Give the extent of all Plasmodium vivax-infected red blood cells.
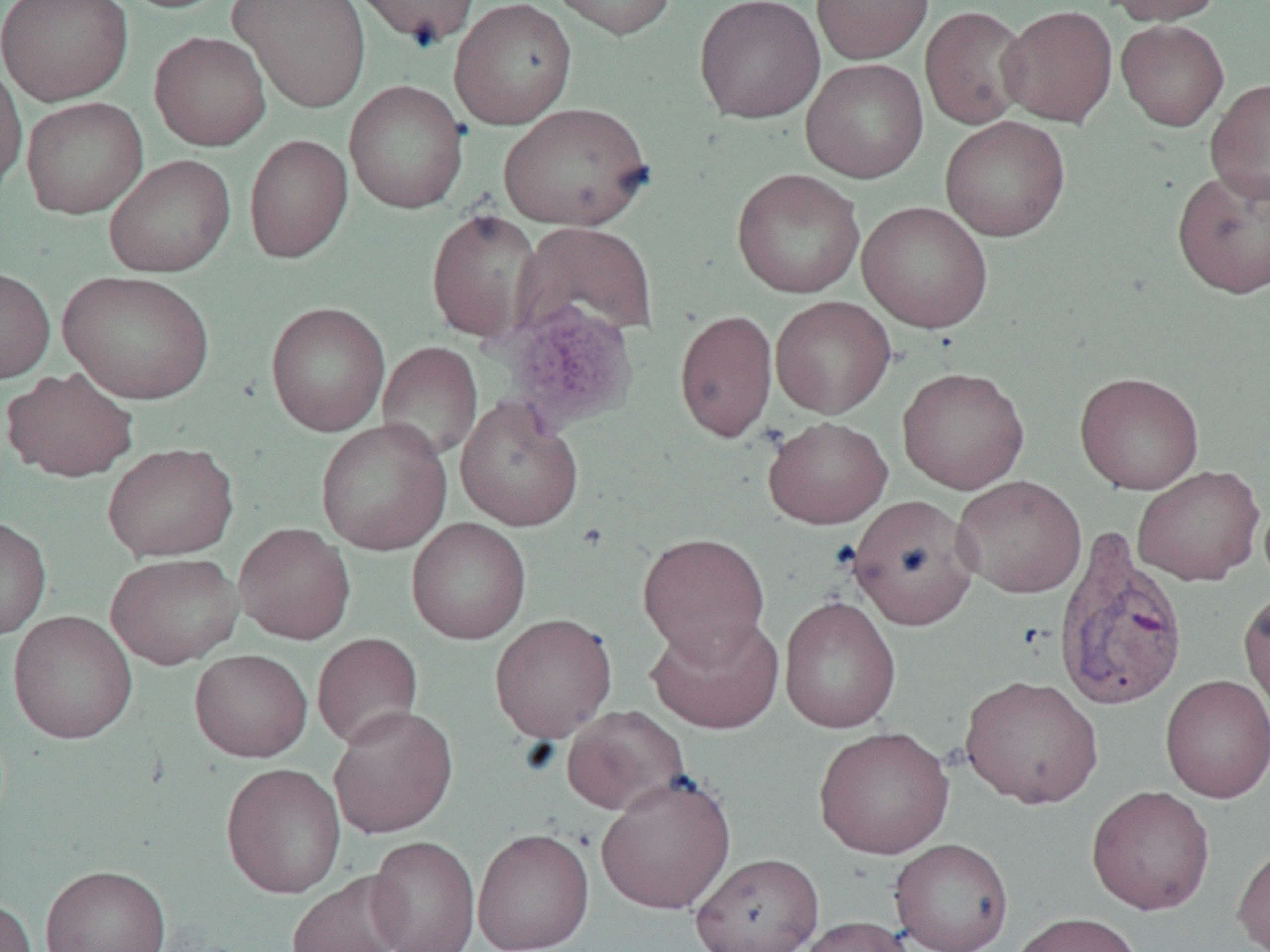

Approximate bounding boxes as [x1, y1, x2, y2] in pixels.
Plasmodium vivax-infected red blood cells: [1053, 529, 1189, 712].

Summary:
  - Platelet locations: [499, 301, 641, 434]
  - Uninfected red blood cell locations: [1, 0, 133, 106], [112, 0, 237, 14], [228, 0, 372, 114], [346, 0, 481, 48], [448, 0, 577, 129], [545, 0, 678, 40], [694, 0, 825, 124], [811, 0, 934, 63], [1103, 0, 1224, 25], [920, 5, 1032, 130], [998, 5, 1118, 127], [1116, 19, 1229, 131], [149, 31, 271, 151], [800, 58, 928, 183], [0, 59, 27, 196], [1205, 78, 1270, 204], [344, 80, 469, 214], [21, 97, 149, 219], [497, 102, 655, 231], [939, 115, 1071, 241], [244, 134, 353, 263], [104, 154, 235, 277], [1171, 166, 1270, 299], [731, 168, 865, 299], [856, 201, 993, 333], [426, 207, 543, 344], [513, 221, 659, 344], [0, 266, 55, 383], [58, 270, 216, 404], [770, 296, 896, 418], [265, 301, 390, 436], [674, 310, 778, 443], [377, 342, 483, 464], [897, 366, 1030, 494], [2, 367, 139, 482], [1074, 371, 1204, 494], [455, 398, 584, 532], [762, 416, 893, 529], [315, 418, 451, 556], [102, 442, 239, 562], [1132, 465, 1265, 586], [952, 475, 1086, 598], [847, 494, 981, 630], [0, 516, 52, 640], [406, 518, 531, 644], [234, 522, 356, 644], [637, 532, 771, 661], [105, 552, 245, 670], [1238, 586, 1270, 719], [779, 595, 901, 733], [7, 610, 138, 745], [489, 612, 617, 742], [646, 613, 784, 734], [312, 633, 424, 750], [189, 649, 313, 762], [960, 674, 1104, 810], [1160, 674, 1270, 804], [328, 705, 458, 839], [561, 705, 691, 816], [814, 726, 954, 859], [221, 762, 346, 898], [596, 773, 736, 915], [1086, 785, 1216, 915], [472, 827, 594, 952], [367, 835, 480, 952], [889, 838, 1014, 952], [1232, 839, 1270, 952], [690, 852, 823, 952], [41, 864, 171, 952], [286, 871, 408, 952], [0, 897, 37, 952], [1007, 911, 1144, 952], [795, 916, 915, 952]
  - Slide-level diagnosis: Plasmodium vivax
  - Modality: light microscopy
  - Preparation: thin blood smear
  - Field of view: one of a larger specimen
  - Image size: 1270×952 pixels
  - Magnification: 1000x